Assess the morphology of the red blood cells.
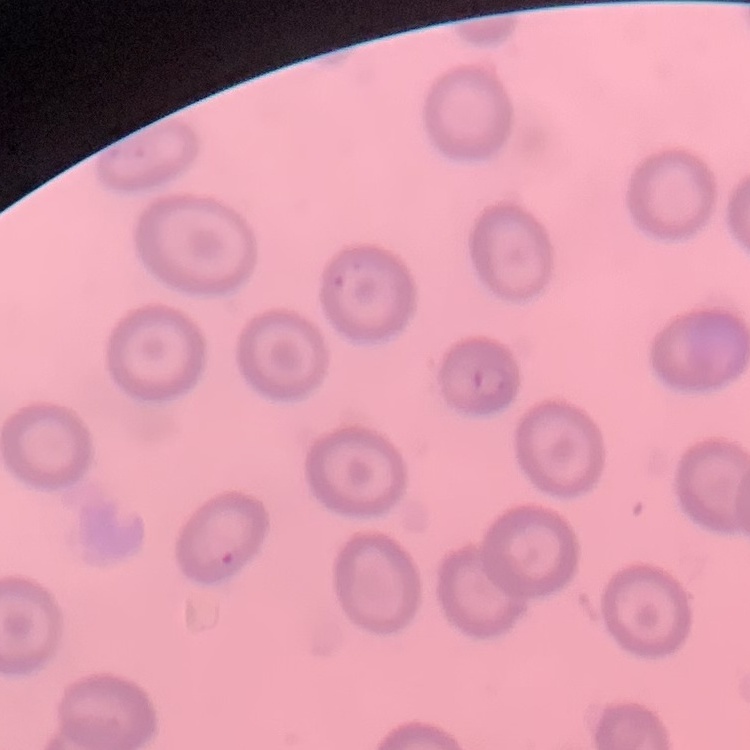

No rouleaux formation.

Summary:
  - Preparation: thin blood smear
  - Stain: Field's or Giemsa
  - Image type: one tile cut from a larger photomicrograph